Name the parasite shown.
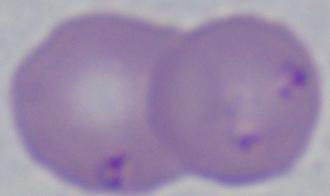

Babesia.

Summary:
  - Magnification: 1000x
  - Modality: micrograph